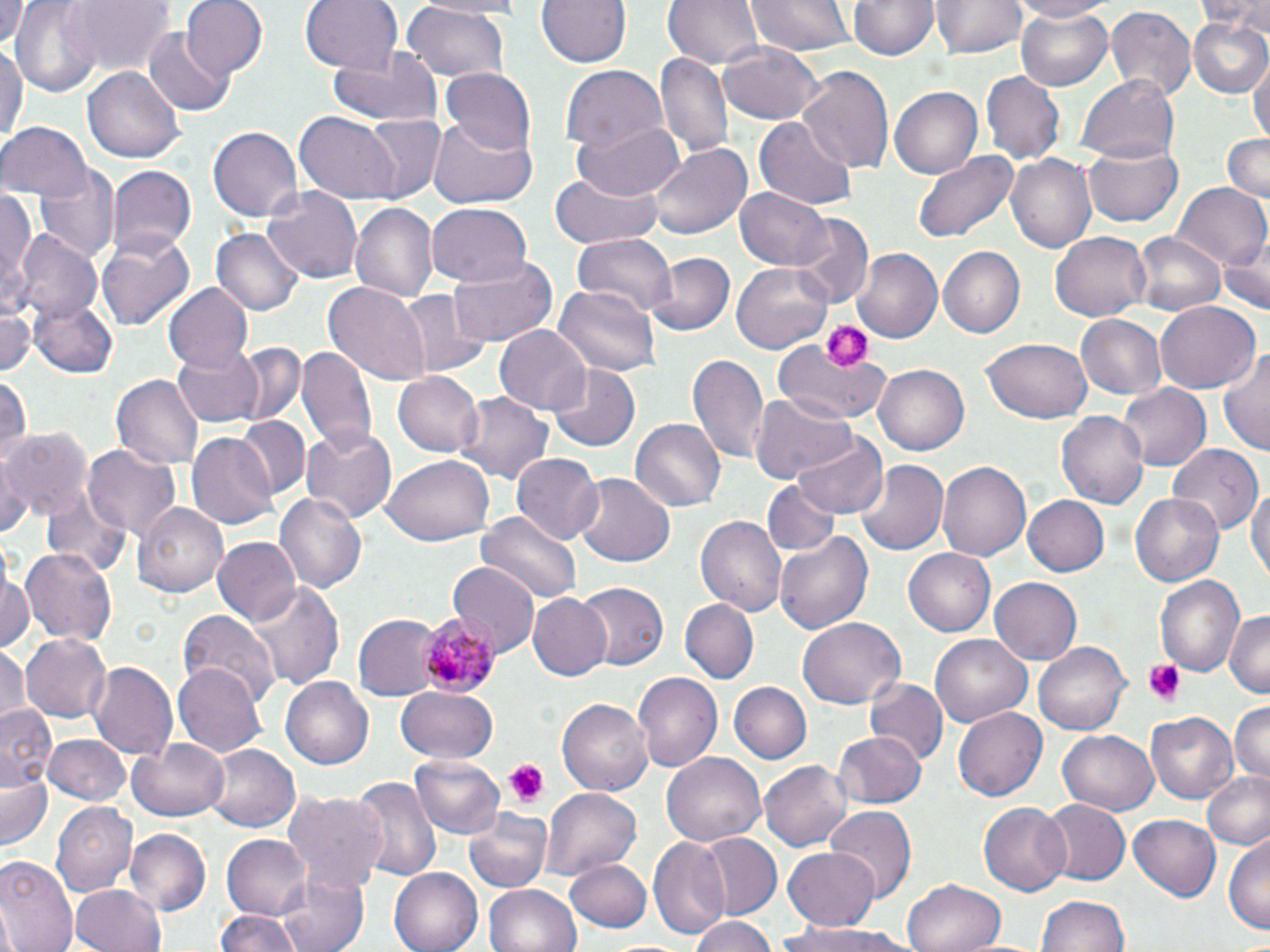

slide-level diagnosis = Plasmodium malariae
stain = May-Grünwald-Giemsa
modality = optical microscopy
platelet locations = approximate bounding boxes as named x1/y1/x2/y2 corners in pixels: (x1=820, y1=320, x2=871, y2=371), (x1=1142, y1=658, x2=1188, y2=704), (x1=506, y1=761, x2=550, y2=805)
magnification = 1000x
field of view = one of a larger specimen
preparation = thin blood smear
Plasmodium malariae-infected red blood cell locations = approximate bounding boxes as named x1/y1/x2/y2 corners in pixels: (x1=418, y1=614, x2=493, y2=696)
uninfected red blood cell locations = approximate bounding boxes as named x1/y1/x2/y2 corners in pixels: (x1=12, y1=0, x2=101, y2=92), (x1=61, y1=0, x2=173, y2=79), (x1=181, y1=0, x2=268, y2=79), (x1=301, y1=0, x2=404, y2=77), (x1=538, y1=0, x2=629, y2=68), (x1=664, y1=0, x2=764, y2=69), (x1=747, y1=0, x2=852, y2=56), (x1=847, y1=0, x2=938, y2=61), (x1=1011, y1=0, x2=1111, y2=22), (x1=1198, y1=0, x2=1270, y2=36), (x1=1, y1=1, x2=32, y2=52), (x1=932, y1=1, x2=1025, y2=59), (x1=400, y1=4, x2=510, y2=82), (x1=1104, y1=5, x2=1197, y2=101), (x1=1014, y1=9, x2=1117, y2=90), (x1=1186, y1=14, x2=1270, y2=100), (x1=143, y1=27, x2=233, y2=115), (x1=0, y1=39, x2=25, y2=149), (x1=720, y1=39, x2=823, y2=124), (x1=332, y1=46, x2=441, y2=127), (x1=655, y1=53, x2=734, y2=165), (x1=1250, y1=58, x2=1270, y2=148), (x1=84, y1=65, x2=183, y2=163), (x1=561, y1=65, x2=666, y2=155), (x1=796, y1=66, x2=893, y2=173), (x1=440, y1=67, x2=536, y2=156), (x1=981, y1=70, x2=1065, y2=166), (x1=1081, y1=73, x2=1180, y2=164), (x1=892, y1=85, x2=986, y2=179), (x1=294, y1=112, x2=400, y2=204), (x1=359, y1=113, x2=447, y2=201), (x1=426, y1=116, x2=539, y2=209), (x1=756, y1=118, x2=856, y2=209), (x1=1, y1=119, x2=90, y2=201), (x1=570, y1=121, x2=685, y2=200), (x1=208, y1=125, x2=304, y2=223), (x1=1220, y1=132, x2=1270, y2=205), (x1=1085, y1=139, x2=1183, y2=226), (x1=650, y1=143, x2=752, y2=239), (x1=913, y1=148, x2=1021, y2=242), (x1=1007, y1=152, x2=1098, y2=254), (x1=106, y1=164, x2=196, y2=263), (x1=34, y1=165, x2=118, y2=265), (x1=547, y1=172, x2=664, y2=249), (x1=1171, y1=182, x2=1270, y2=274), (x1=0, y1=185, x2=36, y2=313), (x1=262, y1=186, x2=363, y2=285), (x1=737, y1=187, x2=833, y2=270), (x1=349, y1=202, x2=437, y2=304), (x1=426, y1=203, x2=532, y2=288), (x1=792, y1=216, x2=873, y2=305), (x1=212, y1=228, x2=303, y2=316), (x1=98, y1=231, x2=194, y2=331), (x1=1051, y1=232, x2=1152, y2=322), (x1=1131, y1=232, x2=1226, y2=318), (x1=12, y1=233, x2=102, y2=327), (x1=572, y1=234, x2=677, y2=324), (x1=1216, y1=240, x2=1269, y2=316), (x1=938, y1=246, x2=1026, y2=338), (x1=853, y1=248, x2=942, y2=343), (x1=648, y1=252, x2=734, y2=336), (x1=447, y1=255, x2=559, y2=344), (x1=734, y1=260, x2=832, y2=353), (x1=324, y1=282, x2=427, y2=380), (x1=164, y1=284, x2=254, y2=371), (x1=553, y1=286, x2=661, y2=378), (x1=394, y1=289, x2=489, y2=377), (x1=28, y1=296, x2=119, y2=378), (x1=1154, y1=302, x2=1261, y2=395), (x1=0, y1=303, x2=41, y2=377), (x1=1074, y1=314, x2=1168, y2=402), (x1=496, y1=325, x2=592, y2=413), (x1=771, y1=337, x2=893, y2=427), (x1=982, y1=338, x2=1093, y2=424), (x1=171, y1=343, x2=266, y2=426), (x1=221, y1=343, x2=306, y2=427), (x1=296, y1=345, x2=376, y2=453), (x1=1218, y1=346, x2=1270, y2=457), (x1=687, y1=351, x2=769, y2=465), (x1=546, y1=363, x2=640, y2=453), (x1=873, y1=363, x2=970, y2=455), (x1=394, y1=372, x2=484, y2=458), (x1=0, y1=374, x2=29, y2=467), (x1=112, y1=374, x2=205, y2=470), (x1=1120, y1=384, x2=1211, y2=471), (x1=454, y1=391, x2=552, y2=486), (x1=752, y1=393, x2=856, y2=485), (x1=1057, y1=407, x2=1148, y2=507), (x1=236, y1=417, x2=312, y2=499), (x1=630, y1=418, x2=725, y2=513), (x1=301, y1=424, x2=399, y2=519), (x1=5, y1=427, x2=91, y2=522), (x1=794, y1=433, x2=888, y2=518), (x1=186, y1=434, x2=277, y2=530), (x1=1168, y1=443, x2=1262, y2=530), (x1=81, y1=445, x2=183, y2=544), (x1=0, y1=453, x2=27, y2=541), (x1=512, y1=453, x2=603, y2=547), (x1=381, y1=456, x2=494, y2=545), (x1=937, y1=459, x2=1035, y2=561), (x1=858, y1=461, x2=947, y2=557), (x1=573, y1=473, x2=675, y2=568), (x1=761, y1=479, x2=842, y2=559), (x1=1248, y1=480, x2=1269, y2=591), (x1=274, y1=493, x2=368, y2=595), (x1=1128, y1=493, x2=1223, y2=589), (x1=1023, y1=494, x2=1110, y2=577), (x1=135, y1=502, x2=228, y2=599), (x1=477, y1=512, x2=580, y2=606), (x1=696, y1=515, x2=786, y2=618), (x1=775, y1=530, x2=877, y2=635), (x1=214, y1=538, x2=301, y2=627), (x1=22, y1=546, x2=118, y2=644), (x1=902, y1=548, x2=995, y2=637), (x1=1, y1=559, x2=35, y2=654), (x1=448, y1=563, x2=541, y2=653), (x1=1004, y1=573, x2=1102, y2=716), (x1=1154, y1=574, x2=1244, y2=677), (x1=990, y1=578, x2=1082, y2=665), (x1=247, y1=580, x2=343, y2=691), (x1=574, y1=580, x2=668, y2=670), (x1=527, y1=593, x2=612, y2=680), (x1=680, y1=600, x2=758, y2=682), (x1=181, y1=609, x2=278, y2=708), (x1=1223, y1=609, x2=1270, y2=696), (x1=259, y1=611, x2=360, y2=756), (x1=355, y1=615, x2=439, y2=697), (x1=797, y1=618, x2=905, y2=710), (x1=20, y1=634, x2=112, y2=723), (x1=931, y1=635, x2=1031, y2=725), (x1=1035, y1=641, x2=1132, y2=735), (x1=0, y1=644, x2=30, y2=724), (x1=90, y1=661, x2=178, y2=761), (x1=172, y1=662, x2=267, y2=756), (x1=632, y1=673, x2=721, y2=774), (x1=280, y1=677, x2=372, y2=769), (x1=865, y1=677, x2=948, y2=768), (x1=728, y1=681, x2=812, y2=764), (x1=396, y1=685, x2=498, y2=764), (x1=558, y1=698, x2=652, y2=794), (x1=1229, y1=700, x2=1270, y2=785), (x1=1, y1=701, x2=59, y2=792), (x1=955, y1=704, x2=1048, y2=803), (x1=1184, y1=705, x2=1267, y2=793), (x1=1148, y1=710, x2=1238, y2=804), (x1=832, y1=730, x2=927, y2=808), (x1=1057, y1=731, x2=1160, y2=815), (x1=43, y1=734, x2=131, y2=806), (x1=130, y1=740, x2=228, y2=820), (x1=203, y1=745, x2=298, y2=833), (x1=663, y1=752, x2=767, y2=847), (x1=410, y1=753, x2=506, y2=839), (x1=761, y1=759, x2=851, y2=853), (x1=2, y1=768, x2=55, y2=854), (x1=1204, y1=772, x2=1270, y2=848), (x1=352, y1=777, x2=440, y2=884), (x1=545, y1=788, x2=641, y2=877), (x1=285, y1=793, x2=387, y2=892), (x1=1040, y1=799, x2=1128, y2=885), (x1=51, y1=802, x2=135, y2=895), (x1=979, y1=802, x2=1070, y2=896), (x1=824, y1=807, x2=915, y2=897), (x1=464, y1=809, x2=555, y2=894), (x1=1130, y1=814, x2=1221, y2=901), (x1=124, y1=829, x2=209, y2=914), (x1=696, y1=833, x2=782, y2=920), (x1=221, y1=835, x2=311, y2=921), (x1=1226, y1=835, x2=1270, y2=938), (x1=648, y1=837, x2=730, y2=939), (x1=783, y1=846, x2=881, y2=931), (x1=0, y1=853, x2=78, y2=952), (x1=566, y1=859, x2=654, y2=934), (x1=390, y1=866, x2=483, y2=952), (x1=280, y1=870, x2=367, y2=952), (x1=902, y1=877, x2=1006, y2=952), (x1=482, y1=884, x2=581, y2=952), (x1=72, y1=885, x2=166, y2=952), (x1=1037, y1=895, x2=1132, y2=952), (x1=213, y1=909, x2=305, y2=952), (x1=689, y1=917, x2=779, y2=952), (x1=778, y1=920, x2=907, y2=951)
image size = 1270×952 pixels